Identify the cell.
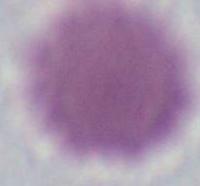
An erythrocyte.

Captured at 1000x magnification. Photomicrograph.